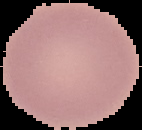

Summary:
  - Preparation: thin blood film
  - Image type: segmented cell region on a black background
  - Image size: 142×130 pixels
  - Result: no malaria parasites seen